Give the extent of all Plasmodium falciparum-infected red blood cells.
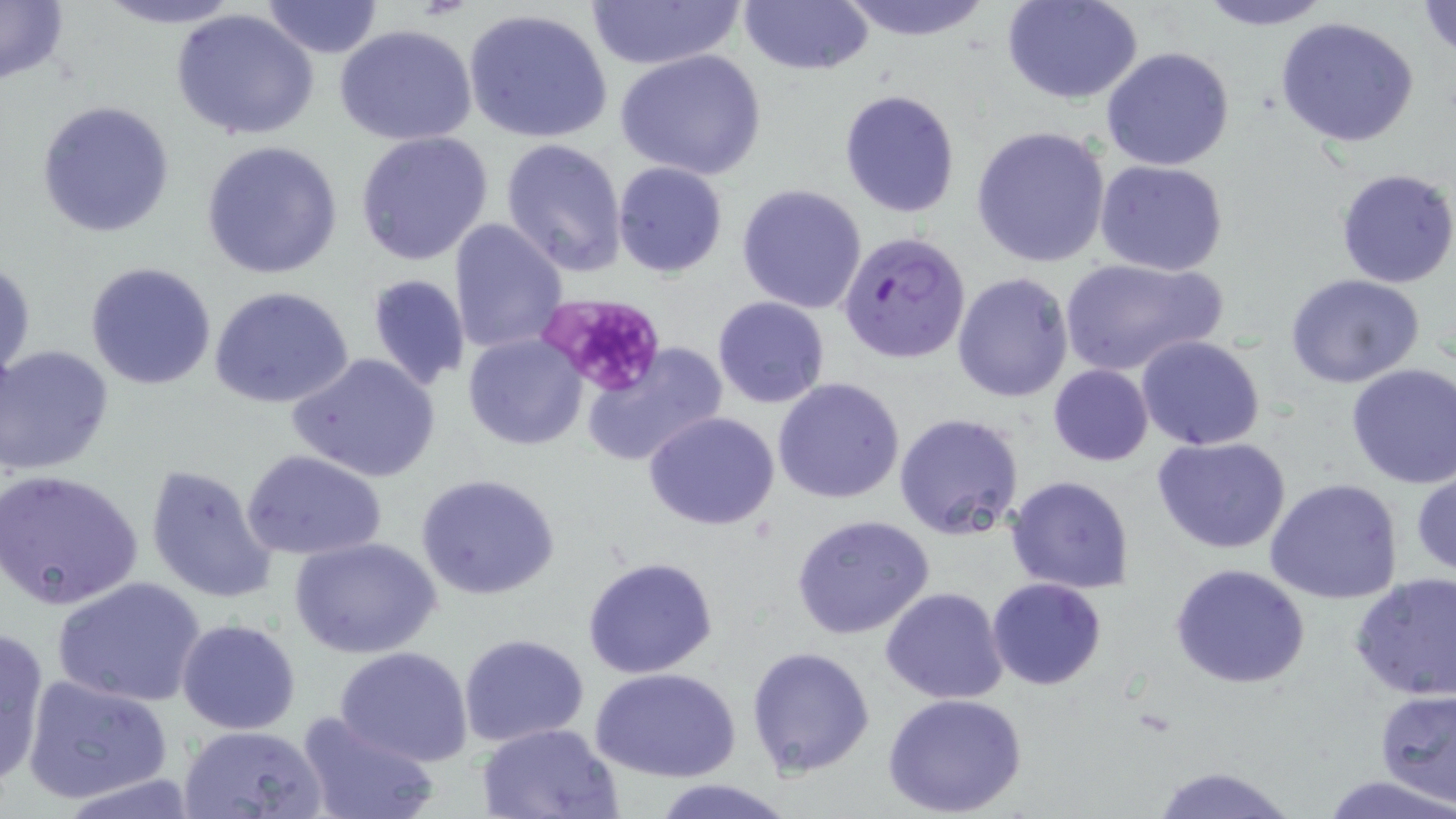
Approximate bounding boxes as [x1, y1, x2, y2] in pixels.
Plasmodium falciparum-infected red blood cells: [840, 231, 970, 362].

Summary:
  - Platelet locations: [544, 296, 666, 395]
  - Uninfected red blood cell locations: [738, 0, 875, 76], [833, 0, 995, 42], [1004, 0, 1144, 104], [1195, 0, 1336, 29], [0, 1, 69, 87], [92, 1, 246, 29], [259, 1, 385, 58], [588, 1, 742, 71], [1416, 1, 1456, 57], [171, 8, 321, 141], [462, 8, 615, 146], [1274, 15, 1421, 148], [333, 23, 480, 148], [1101, 47, 1237, 172], [615, 48, 768, 179], [839, 89, 961, 217], [36, 98, 176, 237], [972, 125, 1111, 268], [355, 131, 493, 265], [500, 138, 629, 277], [202, 140, 342, 280], [1095, 160, 1230, 277], [613, 161, 728, 278], [1335, 168, 1456, 288], [737, 184, 868, 314], [447, 218, 568, 357], [1060, 257, 1227, 377], [1, 259, 36, 386], [85, 262, 217, 391], [1285, 271, 1426, 388], [953, 272, 1074, 404], [365, 273, 472, 391], [208, 285, 355, 409], [712, 296, 830, 408], [716, 317, 857, 472], [464, 332, 589, 451], [1135, 335, 1265, 451], [582, 343, 728, 467], [1, 344, 114, 475], [286, 351, 441, 484], [1345, 362, 1456, 489], [1048, 364, 1154, 466], [773, 377, 906, 504], [644, 412, 781, 530], [893, 412, 1024, 539], [1152, 437, 1294, 555], [243, 451, 387, 561], [143, 463, 278, 603], [1411, 467, 1456, 579], [2, 468, 144, 609], [416, 473, 561, 599], [1006, 475, 1135, 593], [1265, 479, 1404, 604], [792, 515, 936, 640], [290, 535, 443, 660], [582, 557, 719, 679], [1170, 562, 1310, 689], [1349, 572, 1456, 703], [51, 576, 209, 708], [987, 577, 1107, 690], [880, 587, 1009, 705], [176, 617, 302, 735], [0, 626, 50, 785], [459, 634, 588, 749], [334, 645, 476, 767], [747, 645, 875, 778], [592, 666, 741, 782], [23, 673, 173, 806], [1375, 688, 1456, 805], [883, 692, 1029, 817], [295, 709, 440, 819], [477, 721, 625, 819], [179, 725, 327, 818], [1146, 764, 1301, 819], [1320, 773, 1455, 819], [55, 776, 208, 817], [651, 779, 791, 819]
  - Slide-level diagnosis: Plasmodium falciparum
  - Preparation: thin blood smear
  - Image size: 1456×819 pixels
  - Modality: optical microscopy
  - Magnification: 1000x
  - Field of view: one of a larger specimen
  - Stain: May-Grünwald-Giemsa